Identify the parasite.
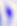
Toxoplasma gondii.

modality: micrograph
magnification: 400x